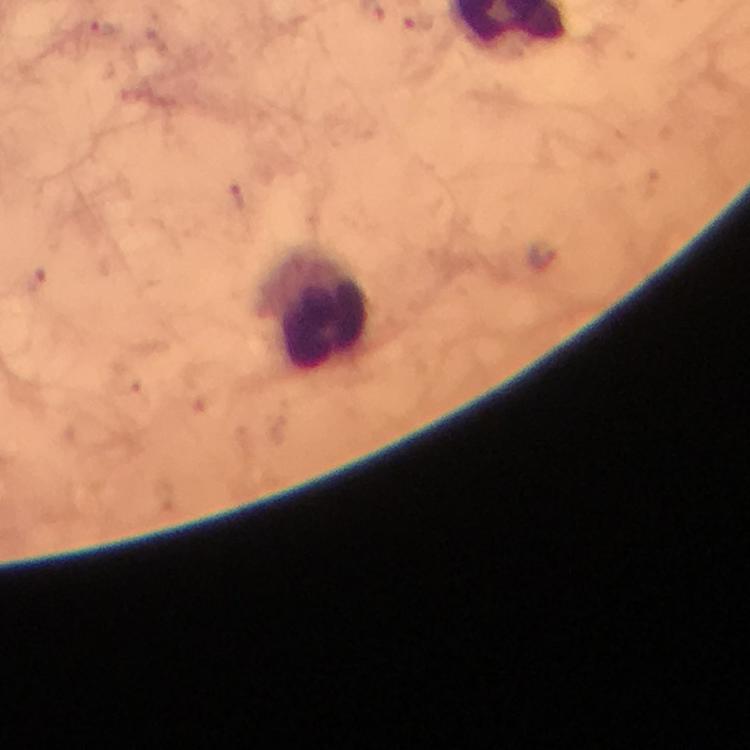

Approximate centers as (x, y) in pixels.
Summary:
  - Plasmodium parasite locations: (418, 24), (544, 256)
  - Leukocyte locations: (317, 310)
  - Image size: 750×750 pixels
  - Immersion oil: applied
  - Preparation: thick blood film
  - Capture: smartphone photograph through a microscope
  - Context: from a malaria diagnostic workup
  - Stain: Giemsa
  - Magnification: 100x
  - Cropped from: a single field of view